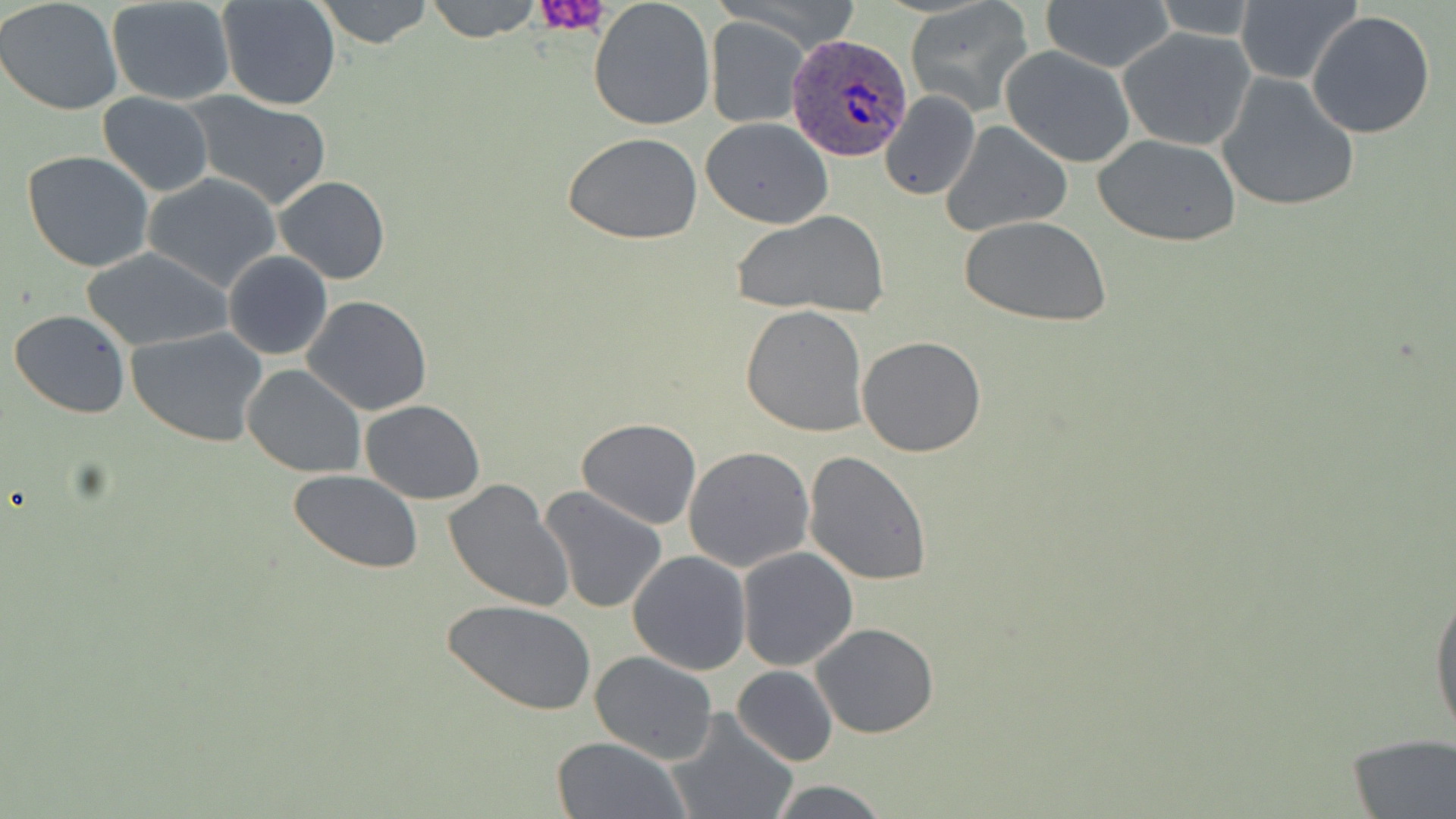

Approximate bounding boxes as [x1, y1, x2, y2] in pixels. Platelet locations: [531, 0, 615, 35]. Plasmodium ovale-infected red blood cell locations: [785, 34, 915, 160]. Uninfected red blood cell locations: [0, 0, 124, 116], [216, 0, 342, 110], [314, 0, 435, 50], [425, 0, 542, 43], [587, 0, 716, 132], [714, 0, 865, 57], [905, 0, 1035, 118], [106, 1, 235, 106], [1042, 1, 1174, 72], [1147, 1, 1260, 39], [1234, 2, 1360, 85], [1307, 10, 1438, 140], [705, 15, 810, 128], [1118, 27, 1255, 149], [1000, 46, 1136, 167], [1216, 73, 1361, 213], [881, 89, 981, 201], [184, 91, 333, 211], [98, 92, 214, 195], [701, 118, 833, 229], [942, 120, 1074, 236], [561, 132, 704, 243], [1092, 133, 1243, 247], [22, 149, 155, 272], [141, 173, 282, 292], [275, 175, 390, 286], [731, 210, 890, 319], [963, 216, 1110, 327], [80, 247, 232, 352], [224, 251, 332, 360], [302, 295, 432, 416], [739, 304, 869, 437], [9, 307, 129, 420], [127, 326, 268, 447], [857, 336, 988, 457], [241, 362, 366, 478], [360, 399, 484, 504], [576, 419, 701, 530], [684, 446, 815, 573], [802, 450, 932, 585], [288, 472, 424, 573], [443, 478, 574, 611], [539, 486, 668, 615], [736, 546, 858, 670], [627, 549, 751, 675], [1429, 564, 1456, 756], [446, 600, 595, 716], [810, 622, 938, 739], [589, 650, 719, 764], [733, 665, 838, 766], [663, 709, 798, 819], [1346, 734, 1456, 817], [550, 736, 690, 819], [765, 779, 890, 818]. Slide-level diagnosis: Plasmodium ovale. Thin blood smear. Captured at 1000x magnification. May-Grünwald-Giemsa-stained preparation. Light microscopy. Single field of view. Image is 1456×819 pixels.